Give the position of every Plasmodium parasite visible.
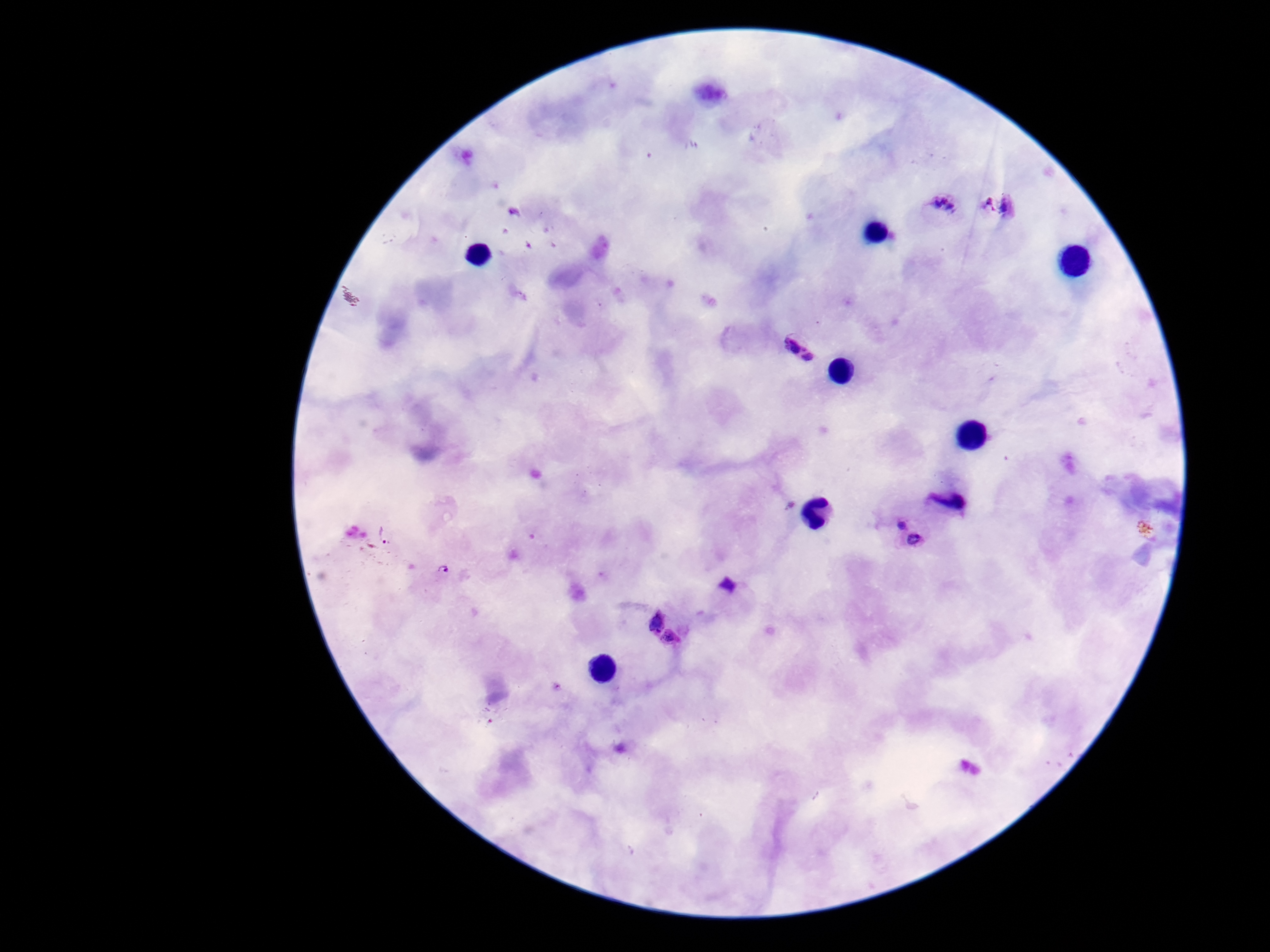

Approximate centers as (x, y) in pixels.
Plasmodium parasites: (942, 206), (1001, 206), (803, 343), (952, 496), (901, 521), (387, 535), (915, 543), (442, 570), (730, 586), (657, 617), (671, 639).

{
  "capture": "smartphone camera through the microscope eyepiece",
  "patient_malaria_status": "infected",
  "preparation": "thick blood smear",
  "field_of_view": "single",
  "magnification": "100x",
  "stain": "Giemsa",
  "image_size": "1270×952 pixels"
}